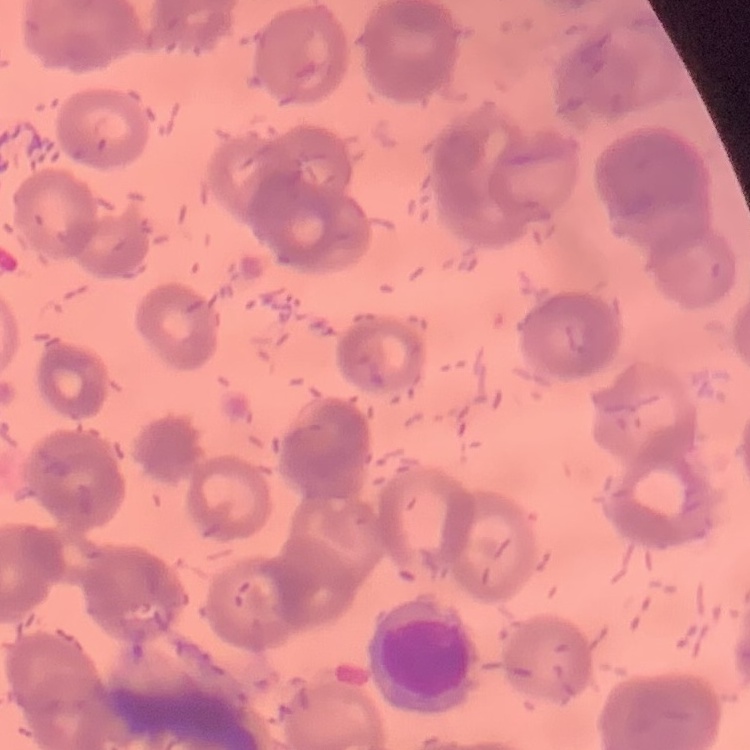

erythrocyte morphology = rouleaux formation
preparation = thin blood smear
image type = square crop of a larger photomicrograph
stain = Field's or Giemsa